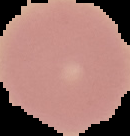

Segmented cell region on a black background. From a thin blood smear. Malaria status: uninfected. Image is 130×136 pixels.